Give the extent of all Plasmodium falciparum-infected red blood cells.
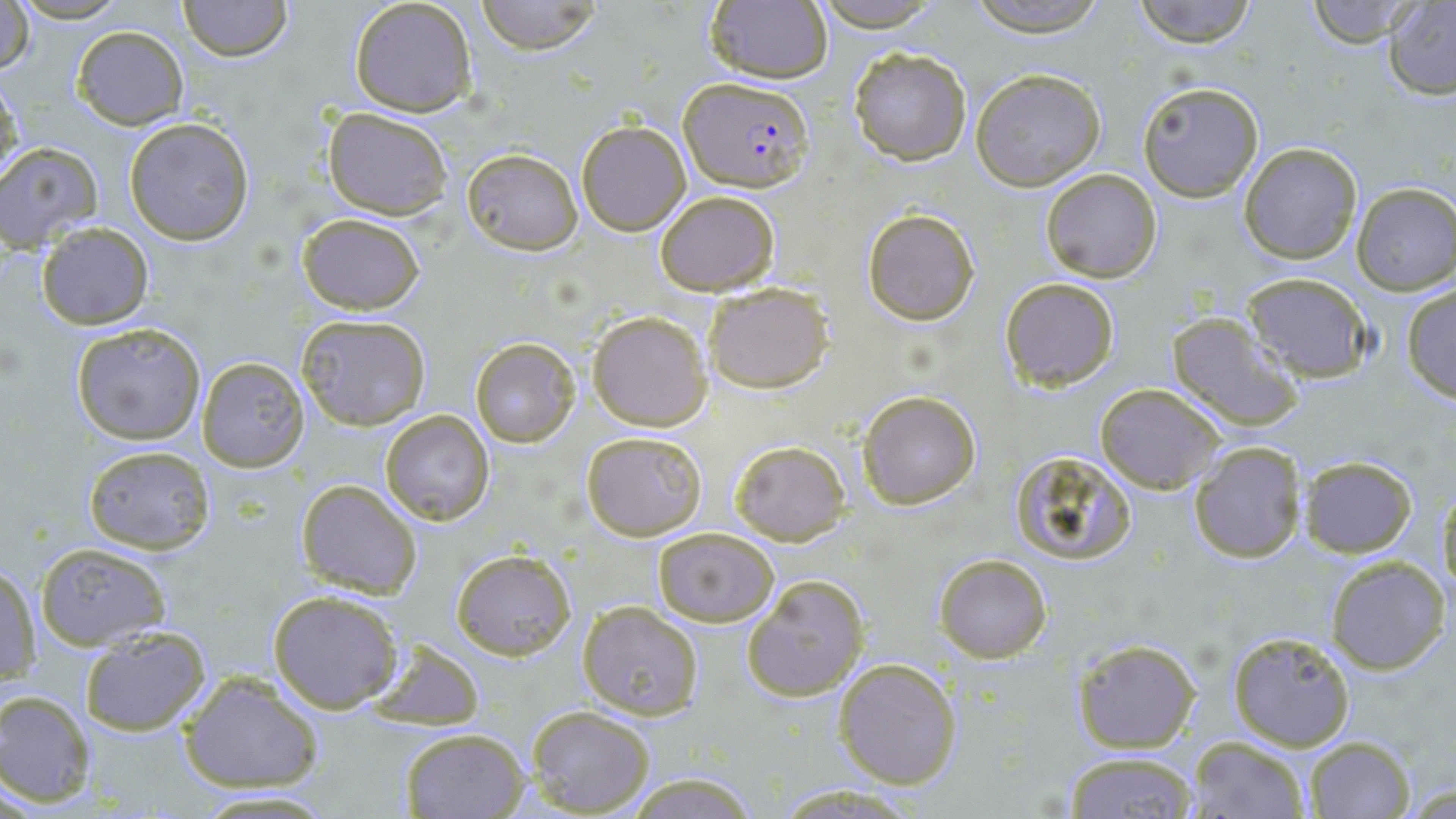
Approximate bounding boxes as (x1,y1)-(x2,y2) corner pairs in pixels.
Plasmodium falciparum-infected red blood cells: (679,76)-(813,193).

slide_level_diagnosis: Plasmodium falciparum
preparation: thin blood film
uninfected_red_blood_cell_locations: 'approximate bounding boxes as (x1,y1)-(x2,y2) corner pairs in pixels: (11,0)-(132,24), (177,0)-(292,62), (348,0)-(479,118), (478,0)-(601,54), (703,0)-(832,87), (809,0)-(947,32), (965,0)-(1111,38), (1131,0)-(1261,47), (1305,0)-(1421,47), (1382,2)-(1456,98), (1,3)-(35,81), (72,25)-(188,130), (846,46)-(971,165), (970,68)-(1108,190), (1,74)-(24,182), (1136,80)-(1264,203), (323,108)-(451,219), (124,117)-(256,245), (576,120)-(690,235), (1239,140)-(1364,265), (0,142)-(102,249), (462,146)-(583,256), (1039,168)-(1163,282), (1352,183)-(1455,296), (654,189)-(779,294), (861,207)-(979,325), (296,211)-(427,314), (37,224)-(153,329), (1242,272)-(1374,383), (999,277)-(1121,391), (703,281)-(835,394), (1400,285)-(1456,402), (588,311)-(712,430), (1165,312)-(1301,433), (296,314)-(432,430), (70,320)-(207,446), (472,338)-(580,446), (197,355)-(311,472), (1095,383)-(1225,494), (858,389)-(982,510), (380,409)-(495,526), (581,429)-(708,540), (729,439)-(849,544), (1187,441)-(1305,565), (83,444)-(216,554), (1009,452)-(1139,566), (1299,455)-(1417,556), (295,478)-(422,598), (1436,483)-(1456,606), (652,527)-(779,626), (34,541)-(173,650), (450,548)-(577,661), (934,552)-(1052,662), (1326,556)-(1449,674), (2,564)-(42,685), (741,573)-(870,702), (267,589)-(403,713), (577,602)-(703,721), (78,626)-(211,737), (1228,630)-(1358,751), (1072,637)-(1200,753), (368,638)-(484,731), (834,658)-(962,789), (177,670)-(324,792), (0,690)-(98,805), (526,706)-(654,817), (399,726)-(530,818), (1185,736)-(1310,819), (1303,736)-(1414,819), (1061,750)-(1199,819), (623,769)-(761,818), (772,785)-(925,817), (183,790)-(341,818)'
magnification: 1000x
image_size: 1456×819 pixels
stain: May-Grünwald-Giemsa
field_of_view: single
modality: optical microscopy